Point out each Plasmodium parasite.
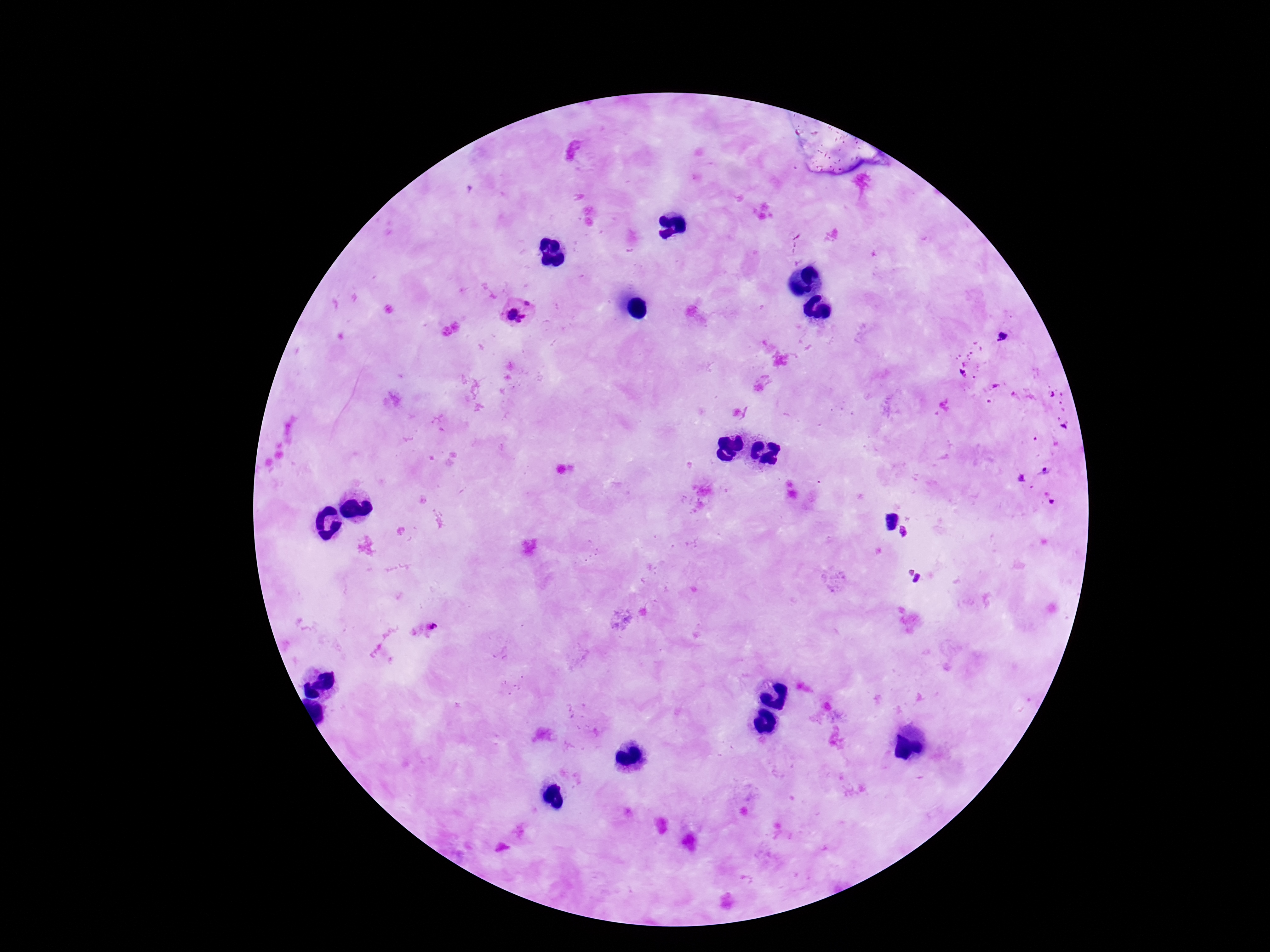
Approximate centers as {x, y} in pixels.
Plasmodium parasites: {527, 304}, {511, 314}, {523, 321}, {1001, 337}, {1044, 471}, {432, 626}.

Summary:
  - Image size: 1270×952 pixels
  - Capture: smartphone camera through the microscope eyepiece
  - Preparation: thick blood film
  - Patient malaria status: positive
  - Stain: Giemsa
  - Magnification: 100x
  - Field of view: one from this slide